Identify the parasite.
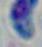
This is Toxoplasma gondii.

1000x magnification. Photomicrograph.